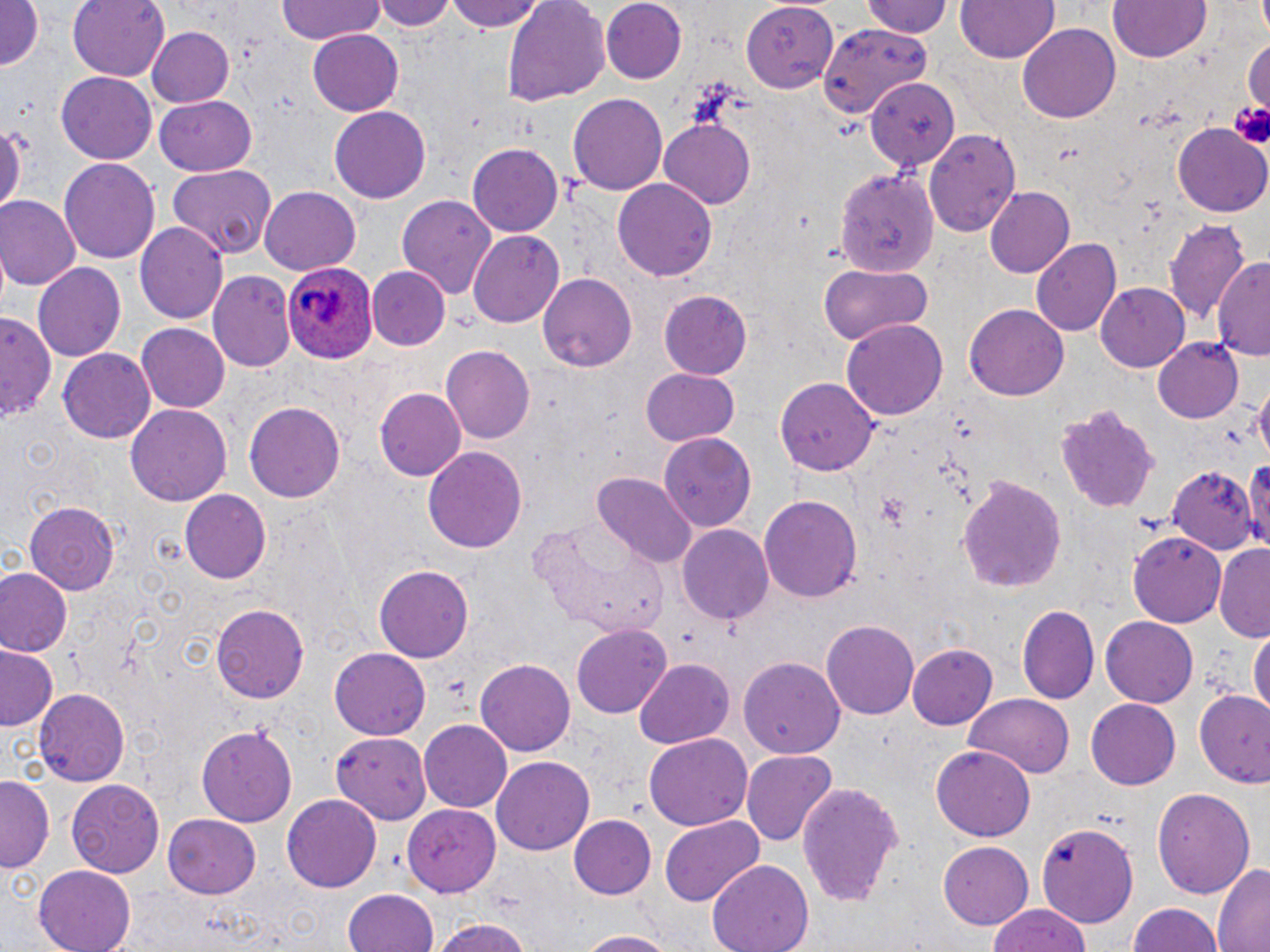

Summary:
  - Coordinate format: approximate bounding boxes as named x1/y1/x2/y2 corners in pixels
  - Plasmodium ovale-infected red blood cell locations: (x1=282, y1=261, x2=379, y2=367)
  - Uninfected red blood cell locations: (x1=69, y1=0, x2=169, y2=78), (x1=274, y1=0, x2=389, y2=49), (x1=375, y1=0, x2=454, y2=32), (x1=447, y1=0, x2=546, y2=32), (x1=501, y1=0, x2=611, y2=107), (x1=600, y1=0, x2=688, y2=84), (x1=863, y1=0, x2=954, y2=38), (x1=954, y1=0, x2=1061, y2=63), (x1=0, y1=1, x2=46, y2=71), (x1=741, y1=1, x2=841, y2=88), (x1=1109, y1=1, x2=1211, y2=64), (x1=817, y1=21, x2=932, y2=112), (x1=1018, y1=23, x2=1121, y2=125), (x1=146, y1=25, x2=237, y2=108), (x1=306, y1=29, x2=405, y2=116), (x1=58, y1=71, x2=157, y2=163), (x1=868, y1=76, x2=956, y2=172), (x1=567, y1=93, x2=667, y2=195), (x1=154, y1=95, x2=256, y2=176), (x1=328, y1=106, x2=432, y2=204), (x1=0, y1=116, x2=29, y2=221), (x1=661, y1=119, x2=755, y2=207), (x1=1173, y1=124, x2=1269, y2=218), (x1=925, y1=128, x2=1022, y2=236), (x1=467, y1=143, x2=563, y2=236), (x1=59, y1=157, x2=161, y2=265), (x1=165, y1=165, x2=276, y2=260), (x1=835, y1=166, x2=936, y2=276), (x1=613, y1=178, x2=719, y2=282), (x1=260, y1=187, x2=360, y2=274), (x1=983, y1=187, x2=1074, y2=279), (x1=395, y1=192, x2=497, y2=300), (x1=0, y1=198, x2=79, y2=292), (x1=1164, y1=220, x2=1249, y2=328), (x1=136, y1=222, x2=227, y2=324), (x1=468, y1=229, x2=565, y2=326), (x1=1030, y1=238, x2=1123, y2=334), (x1=1213, y1=255, x2=1270, y2=359), (x1=33, y1=262, x2=127, y2=363), (x1=817, y1=264, x2=934, y2=346), (x1=368, y1=266, x2=449, y2=350), (x1=207, y1=270, x2=296, y2=373), (x1=539, y1=272, x2=638, y2=371), (x1=1097, y1=283, x2=1193, y2=371), (x1=659, y1=291, x2=753, y2=379), (x1=965, y1=304, x2=1068, y2=400), (x1=2, y1=313, x2=59, y2=424), (x1=842, y1=320, x2=947, y2=420), (x1=136, y1=322, x2=229, y2=411), (x1=1152, y1=334, x2=1244, y2=422), (x1=440, y1=345, x2=533, y2=444), (x1=57, y1=347, x2=155, y2=442), (x1=642, y1=367, x2=739, y2=445), (x1=774, y1=377, x2=883, y2=478), (x1=374, y1=388, x2=465, y2=482), (x1=245, y1=401, x2=344, y2=505), (x1=1051, y1=401, x2=1164, y2=512), (x1=126, y1=404, x2=231, y2=507), (x1=661, y1=430, x2=757, y2=531), (x1=423, y1=447, x2=529, y2=556), (x1=1245, y1=449, x2=1270, y2=558), (x1=1167, y1=466, x2=1256, y2=555), (x1=595, y1=473, x2=694, y2=567), (x1=957, y1=474, x2=1069, y2=592), (x1=180, y1=490, x2=271, y2=583), (x1=758, y1=492, x2=862, y2=604), (x1=25, y1=501, x2=120, y2=596), (x1=528, y1=521, x2=671, y2=638), (x1=677, y1=523, x2=774, y2=625), (x1=1130, y1=532, x2=1227, y2=629), (x1=1213, y1=544, x2=1270, y2=640), (x1=374, y1=564, x2=471, y2=664), (x1=1, y1=567, x2=70, y2=656), (x1=211, y1=604, x2=309, y2=705), (x1=1017, y1=607, x2=1098, y2=706), (x1=1100, y1=617, x2=1197, y2=707), (x1=822, y1=621, x2=918, y2=720), (x1=572, y1=623, x2=673, y2=718), (x1=1250, y1=628, x2=1270, y2=722), (x1=908, y1=642, x2=1000, y2=730), (x1=1, y1=646, x2=62, y2=731), (x1=328, y1=647, x2=430, y2=740), (x1=740, y1=657, x2=847, y2=761), (x1=477, y1=658, x2=577, y2=755), (x1=634, y1=660, x2=734, y2=747), (x1=35, y1=686, x2=132, y2=785), (x1=965, y1=693, x2=1076, y2=778), (x1=1196, y1=693, x2=1270, y2=790), (x1=1086, y1=697, x2=1181, y2=787), (x1=419, y1=720, x2=513, y2=813), (x1=195, y1=723, x2=297, y2=827), (x1=331, y1=732, x2=433, y2=825), (x1=643, y1=733, x2=752, y2=832), (x1=931, y1=743, x2=1035, y2=840), (x1=742, y1=749, x2=836, y2=846), (x1=493, y1=756, x2=595, y2=856), (x1=2, y1=776, x2=55, y2=874), (x1=67, y1=780, x2=165, y2=879), (x1=798, y1=782, x2=905, y2=905), (x1=1151, y1=787, x2=1258, y2=899), (x1=282, y1=793, x2=382, y2=893), (x1=402, y1=803, x2=501, y2=896), (x1=161, y1=813, x2=262, y2=898), (x1=567, y1=814, x2=655, y2=900), (x1=662, y1=815, x2=765, y2=905), (x1=1035, y1=821, x2=1138, y2=928), (x1=937, y1=840, x2=1035, y2=930), (x1=705, y1=858, x2=815, y2=952), (x1=1212, y1=862, x2=1270, y2=951), (x1=33, y1=865, x2=138, y2=952), (x1=344, y1=889, x2=439, y2=952), (x1=1125, y1=901, x2=1227, y2=952), (x1=989, y1=905, x2=1091, y2=952), (x1=429, y1=917, x2=538, y2=952), (x1=571, y1=929, x2=683, y2=951)
  - Platelet locations: (x1=1231, y1=100, x2=1270, y2=146)
  - Slide-level diagnosis: Plasmodium ovale
  - Preparation: thin blood film
  - Modality: light microscopy
  - Field of view: single
  - Image size: 1270×952 pixels
  - Magnification: 1000x
  - Stain: May-Grünwald-Giemsa